Classify this cell by malaria status.
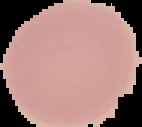
Uninfected.

image type = segmented cell region on a black background
image size = 142×127 pixels
preparation = thin blood film